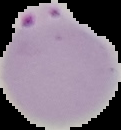
From a thin blood film. The area outside the segmented cell region is set to black. Image is 121×130 pixels. Result: malaria parasites identified.